Identify the blood parasite species.
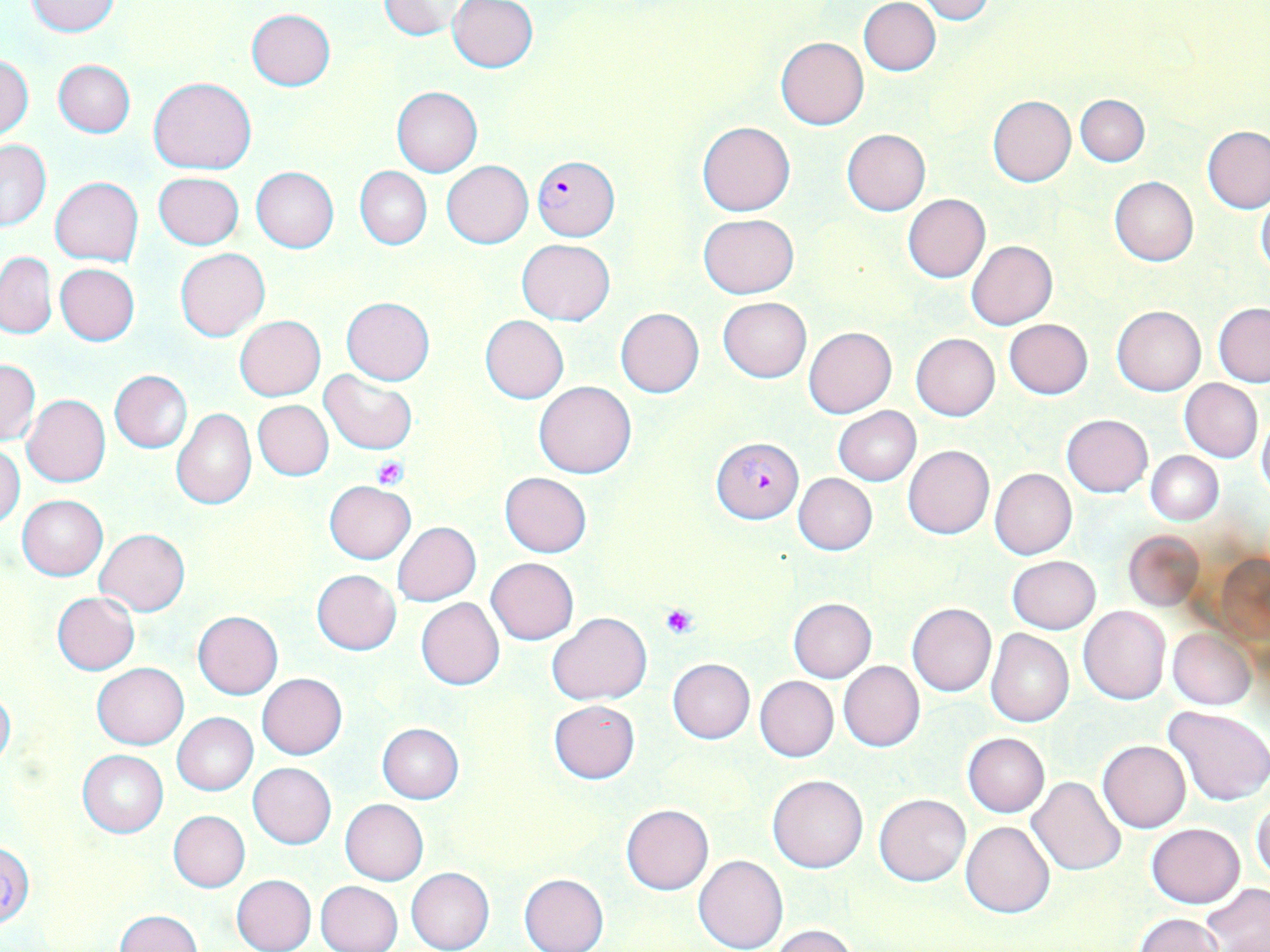

Plasmodium falciparum.

Summary:
  - Coordinate format: approximate bounding boxes as (x1, y1, x2, y2) in pixels
  - Uninfected red blood cell locations: (917, 0, 996, 24), (25, 1, 122, 36), (378, 1, 469, 40), (447, 1, 539, 73), (859, 1, 940, 76), (246, 8, 335, 89), (775, 37, 869, 130), (0, 54, 34, 138), (53, 60, 135, 138), (148, 76, 256, 173), (392, 86, 483, 177), (1076, 94, 1149, 167), (988, 95, 1076, 186), (697, 121, 796, 216), (1202, 126, 1270, 214), (842, 129, 930, 215), (0, 138, 51, 231), (442, 161, 533, 248), (251, 167, 338, 252), (354, 167, 431, 249), (153, 172, 244, 249), (50, 176, 144, 265), (1109, 177, 1198, 265), (903, 193, 991, 281), (1255, 193, 1270, 277), (698, 214, 799, 297), (516, 239, 615, 325), (966, 239, 1057, 329), (175, 248, 270, 342), (1, 252, 56, 339), (55, 263, 140, 345), (342, 297, 434, 384), (718, 297, 811, 382), (1213, 303, 1270, 387), (1112, 305, 1206, 395), (615, 308, 704, 398), (480, 315, 569, 404), (234, 316, 325, 401), (1004, 319, 1093, 400), (803, 326, 897, 417), (911, 333, 1000, 420), (1, 359, 40, 445), (108, 369, 193, 452), (319, 371, 417, 453), (1179, 378, 1262, 462), (534, 380, 637, 479), (23, 394, 111, 486), (253, 400, 333, 480), (834, 406, 920, 485), (171, 407, 256, 509), (1256, 411, 1270, 503), (1061, 414, 1153, 497), (0, 445, 24, 529), (903, 445, 994, 539), (1147, 451, 1223, 525), (989, 467, 1078, 559), (499, 471, 592, 557), (793, 472, 877, 555), (325, 480, 414, 563), (17, 494, 107, 579), (393, 521, 481, 605), (94, 528, 190, 615), (1124, 530, 1204, 610), (1213, 553, 1270, 645), (1007, 556, 1100, 634), (486, 557, 579, 645), (312, 569, 401, 655), (52, 591, 140, 674), (415, 597, 505, 690), (787, 597, 877, 682), (907, 602, 996, 696), (1078, 605, 1171, 704), (193, 611, 283, 699), (546, 612, 650, 705), (1168, 628, 1256, 710), (985, 629, 1074, 727), (667, 658, 754, 744), (838, 661, 925, 751), (91, 662, 188, 749), (257, 673, 347, 759), (755, 676, 838, 761), (0, 686, 15, 770), (548, 699, 639, 784), (1164, 705, 1270, 805), (172, 713, 257, 795), (377, 723, 464, 804), (962, 732, 1049, 816), (1098, 740, 1191, 833), (77, 749, 168, 837), (248, 762, 336, 848), (767, 773, 868, 873), (1026, 776, 1126, 877), (875, 793, 971, 885), (1251, 797, 1270, 883), (340, 799, 429, 885), (621, 804, 714, 895), (169, 811, 250, 892), (961, 821, 1055, 918), (1146, 823, 1244, 907), (0, 841, 34, 926), (694, 854, 788, 952), (406, 867, 494, 952), (519, 873, 608, 952), (231, 874, 316, 952), (315, 880, 403, 952), (1201, 884, 1270, 950), (118, 910, 200, 951), (1134, 914, 1224, 952), (770, 925, 858, 952)
  - Platelet locations: (373, 456, 409, 488), (660, 603, 699, 640)
  - Plasmodium falciparum-infected red blood cell locations: (532, 153, 620, 241), (711, 436, 804, 524)
  - Field of view: single
  - Preparation: thin blood film
  - Image size: 1270×952 pixels
  - Magnification: 1000x
  - Modality: optical microscopy
  - Stain: May-Grünwald-Giemsa